Classify the preparation.
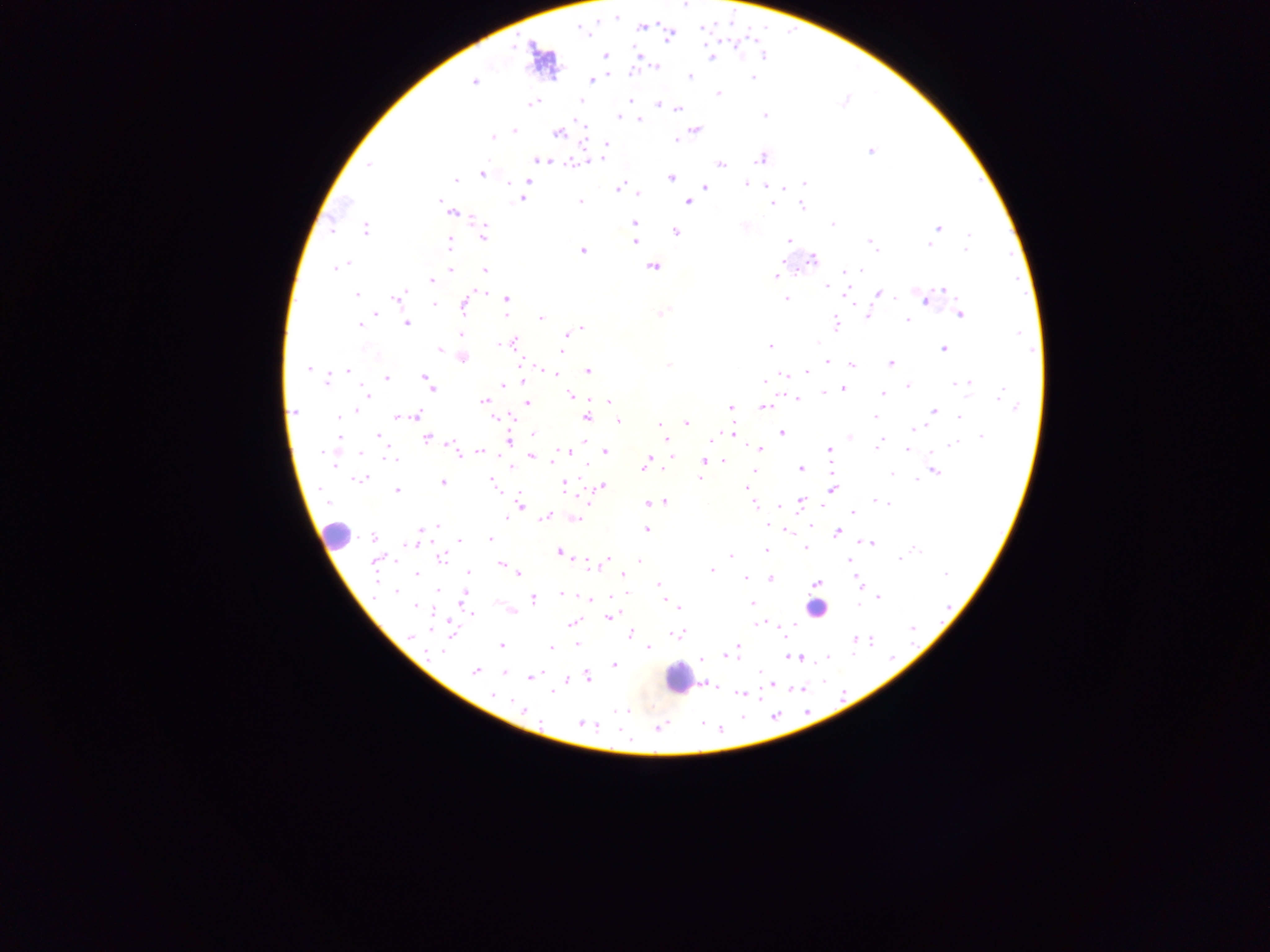

This is a thick smear.

{
  "image_size": "1270×952 pixels",
  "capture": "mobile-phone photograph through a microscope",
  "country": "Ghana",
  "field_of_view": "single",
  "leukocyte_locations": "approximate centers as x y in pixels: 336 535; 811 607; 676 678",
  "plasmodium_parasite_locations": "approximate centers as x y in pixels: 685 5; 615 18; 642 27; 703 28; 580 29; 669 36; 638 54; 605 55; 763 55; 712 57; 656 66; 631 72; 609 75; 690 76; 753 78; 591 80; 473 82; 719 94; 631 100; 580 101; 844 101; 533 103; 658 104; 678 110; 765 115; 618 117; 640 119; 579 123; 696 130; 514 131; 557 134; 493 137; 583 138; 677 141; 607 144; 871 151; 761 158; 601 159; 542 160; 577 162; 720 163; 368 164; 482 174; 671 177; 455 180; 527 181; 803 183; 511 184; 746 184; 619 188; 705 188; 784 188; 638 194; 521 199; 439 200; 580 202; 688 202; 773 205; 801 206; 453 213; 634 223; 833 224; 744 226; 939 228; 331 229; 366 230; 675 232; 969 235; 483 236; 788 241; 870 241; 635 242; 450 243; 929 245; 966 250; 583 251; 813 259; 782 262; 347 263; 336 267; 652 268; 451 269; 485 270; 847 271; 861 271; 776 276; 431 281; 826 287; 944 289; 481 291; 877 293; 846 294; 357 295; 398 298; 506 299; 786 299; 925 300; 435 304; 464 306; 662 313; 375 314; 961 314; 505 315; 868 315; 541 318; 907 320; 359 324; 406 324; 836 324; 581 328; 461 335; 566 335; 818 342; 512 343; 498 345; 564 346; 770 346; 440 349; 944 349; 562 351; 463 358; 827 363; 890 364; 669 365; 852 365; 542 368; 309 369; 347 371; 588 371; 807 372; 556 374; 783 374; 386 378; 426 378; 328 380; 764 381; 957 383; 967 383; 503 385; 431 386; 908 386; 843 389; 824 393; 887 393; 882 394; 571 395; 1000 395; 367 396; 798 399; 484 401; 609 401; 527 402; 731 407; 763 407; 1017 407; 355 411; 933 411; 294 412; 417 416; 339 417; 397 417; 874 417; 959 417; 495 418; 586 418; 618 421; 686 422; 660 424; 915 428; 782 432; 732 433; 533 434; 378 435; 981 436; 850 437; 340 438; 427 438; 712 439; 666 440; 585 441; 509 442; 879 444; 952 444; 451 445; 878 448; 829 449; 760 450; 907 450; 480 451; 568 451; 606 452; 323 453; 360 453; 531 456; 391 459; 705 461; 723 461; 552 462; 646 463; 334 465; 586 465; 510 467; 801 469; 754 471; 934 472; 891 473; 700 478; 916 479; 359 480; 491 480; 442 482; 564 486; 603 486; 747 488; 496 490; 832 490; 397 491; 665 501; 802 501; 876 501; 327 502; 882 502; 654 503; 886 503; 648 504; 753 504; 520 505; 854 512; 545 517; 506 518; 575 519; 767 524; 437 526; 812 526; 783 528; 422 529; 647 530; 787 530; 838 533; 373 537; 418 539; 459 539; 490 539; 868 542; 414 544; 806 547; 766 550; 917 550; 558 552; 730 555; 442 558; 900 558; 607 559; 639 560; 848 560; 376 561; 501 564; 591 567; 711 570; 468 573; 416 574; 946 574; 519 575; 623 575; 745 578; 770 578; 817 583; 858 583; 658 585; 438 591; 395 593; 561 593; 464 596; 879 597; 587 598; 533 599; 664 600; 751 603; 858 604; 416 607; 679 608; 472 615; 614 615; 609 618; 570 623; 757 624; 793 625; 912 628; 630 634; 677 635; 411 637; 854 640; 871 641; 577 644; 501 645; 737 647; 551 648; 648 648; 443 651; 727 656; 795 657; 827 657; 701 659; 614 665; 475 671; 504 672; 759 672; 540 673; 529 677; 588 677; 567 681; 714 685; 553 692; 493 694; 740 694; 511 702; 524 710; 619 711; 580 722; 597 725; 658 728"
}